Identify the cell.
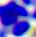

A leukocyte.

Summary:
  - Magnification: 400x
  - Modality: micrograph